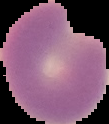
image size = 109×124 pixels
malaria status = parasitized
preparation = thin blood smear
image type = segmented cell region on a black background